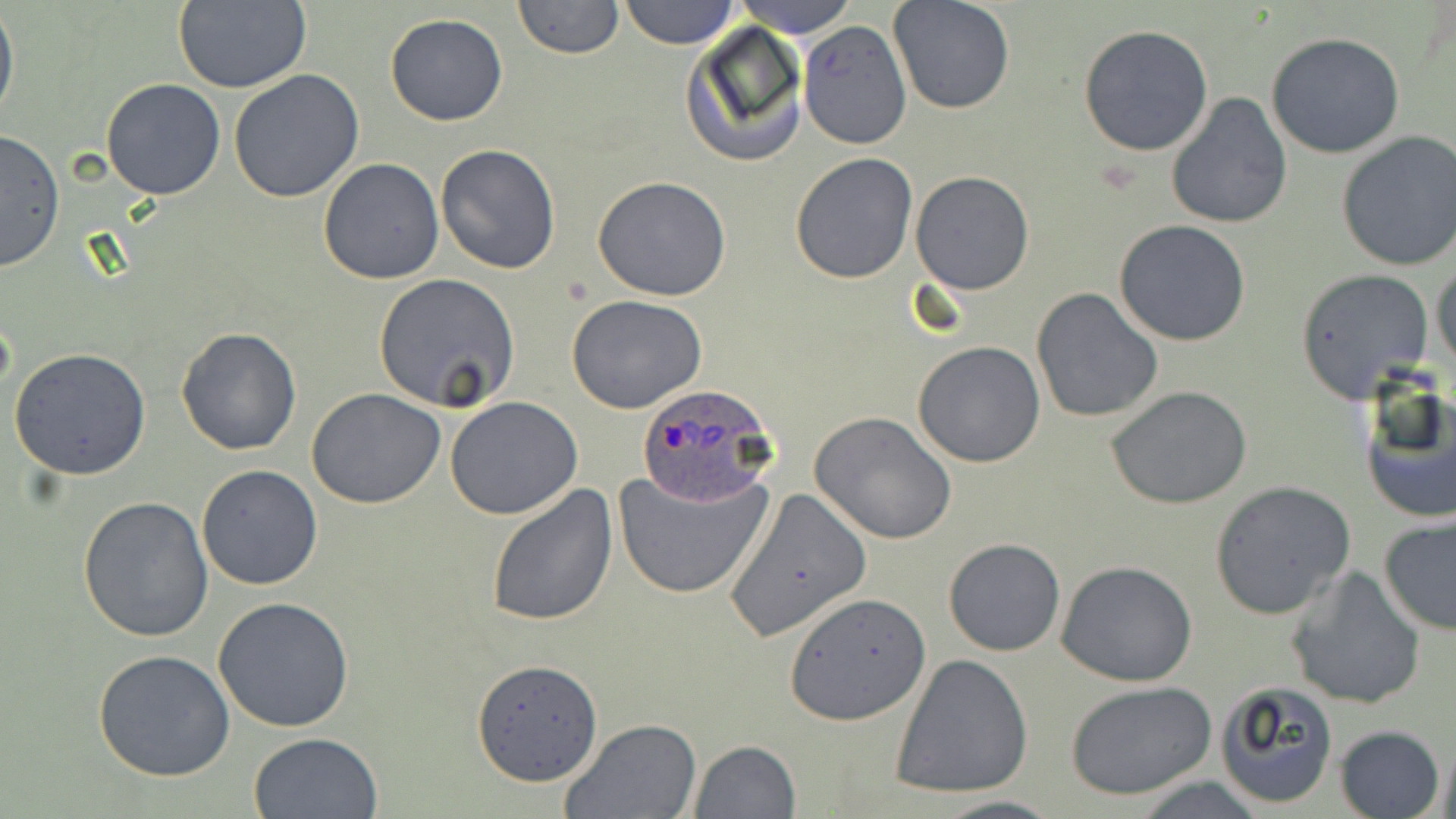

Summary:
  - Coordinate format: approximate bounding boxes as [x1, y1, x2, y2] in pixels
  - Uninfected red blood cell locations: [513, 0, 623, 60], [617, 0, 739, 48], [729, 0, 859, 36], [888, 0, 1016, 115], [172, 2, 312, 92], [0, 5, 19, 127], [384, 14, 508, 125], [797, 21, 912, 150], [681, 23, 810, 168], [1079, 23, 1214, 157], [1265, 32, 1404, 159], [228, 69, 364, 203], [101, 78, 227, 201], [1166, 94, 1292, 230], [0, 129, 65, 272], [1335, 131, 1455, 272], [435, 144, 562, 274], [789, 152, 918, 285], [317, 157, 445, 285], [911, 171, 1035, 294], [591, 175, 734, 301], [1113, 220, 1252, 347], [1431, 258, 1455, 377], [1293, 268, 1436, 402], [373, 273, 520, 413], [1031, 288, 1164, 423], [566, 294, 708, 414], [176, 327, 302, 457], [912, 342, 1045, 467], [9, 348, 153, 481], [1356, 378, 1455, 526], [1106, 385, 1252, 509], [307, 388, 447, 509], [445, 397, 585, 519], [810, 410, 958, 544], [196, 464, 324, 591], [613, 465, 774, 601], [1209, 480, 1356, 619], [486, 484, 618, 627], [722, 486, 871, 642], [78, 494, 212, 640], [1378, 516, 1456, 637], [943, 538, 1066, 657], [1056, 561, 1200, 687], [1285, 566, 1428, 710], [788, 591, 930, 723], [212, 596, 355, 733], [93, 649, 235, 781], [892, 652, 1034, 799], [471, 658, 605, 786], [1065, 680, 1215, 800], [1213, 681, 1339, 811], [560, 718, 704, 819], [1334, 724, 1445, 819], [248, 731, 384, 818], [689, 740, 800, 819], [1124, 775, 1272, 818], [926, 794, 1066, 819]
  - Plasmodium ovale-infected red blood cell locations: [636, 383, 779, 506]
  - Slide-level diagnosis: Plasmodium ovale
  - Field of view: single
  - Preparation: thin blood smear
  - Modality: optical microscopy
  - Magnification: 1000x
  - Image size: 1456×819 pixels
  - Stain: May-Grünwald-Giemsa